State the preparation type.
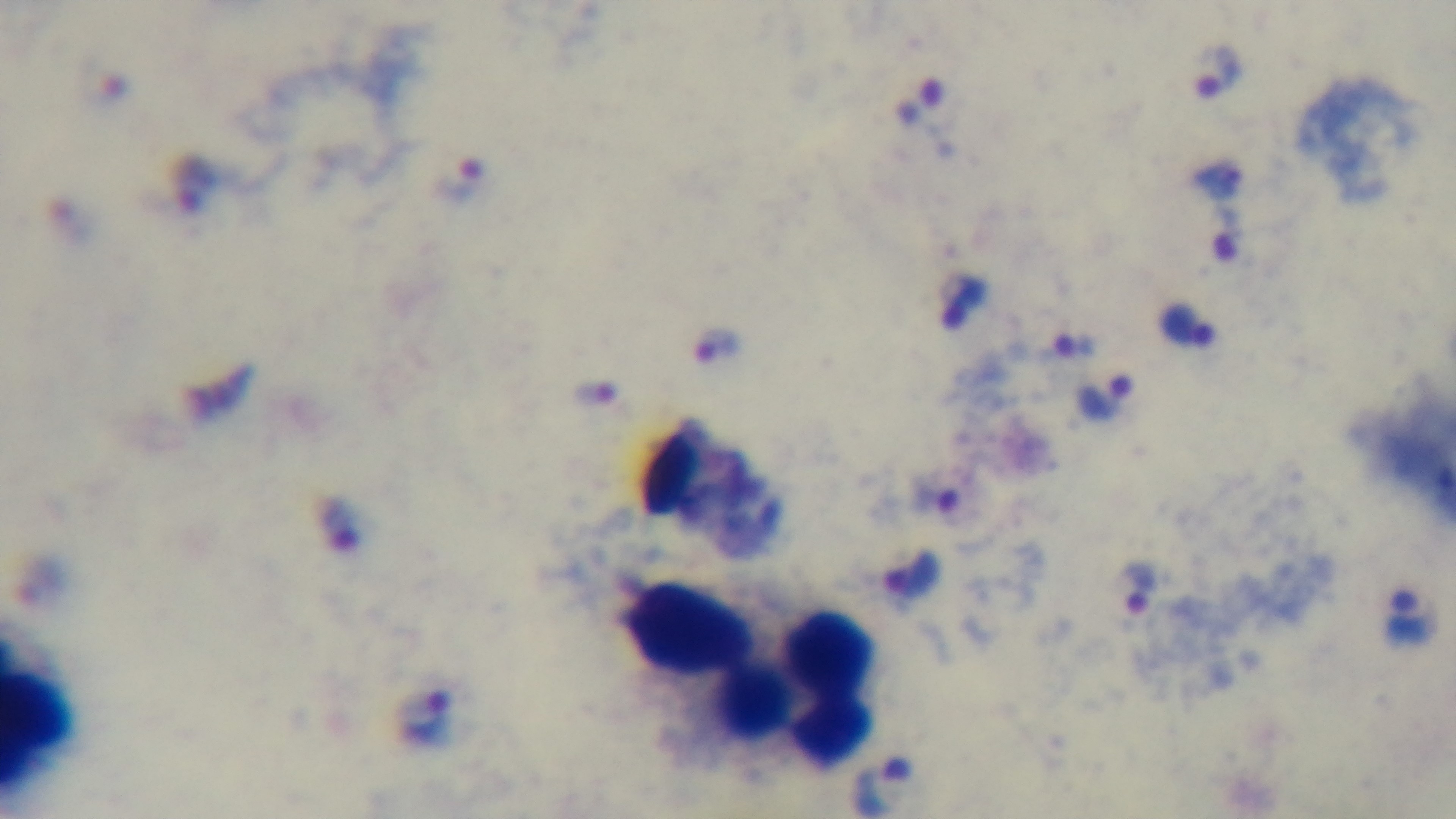
A thick smear.

field_of_view: single
malaria_status: positive
modality: light microscopy
objective: 100x oil immersion
capture: mounted 4K digital camera
stain: Giemsa